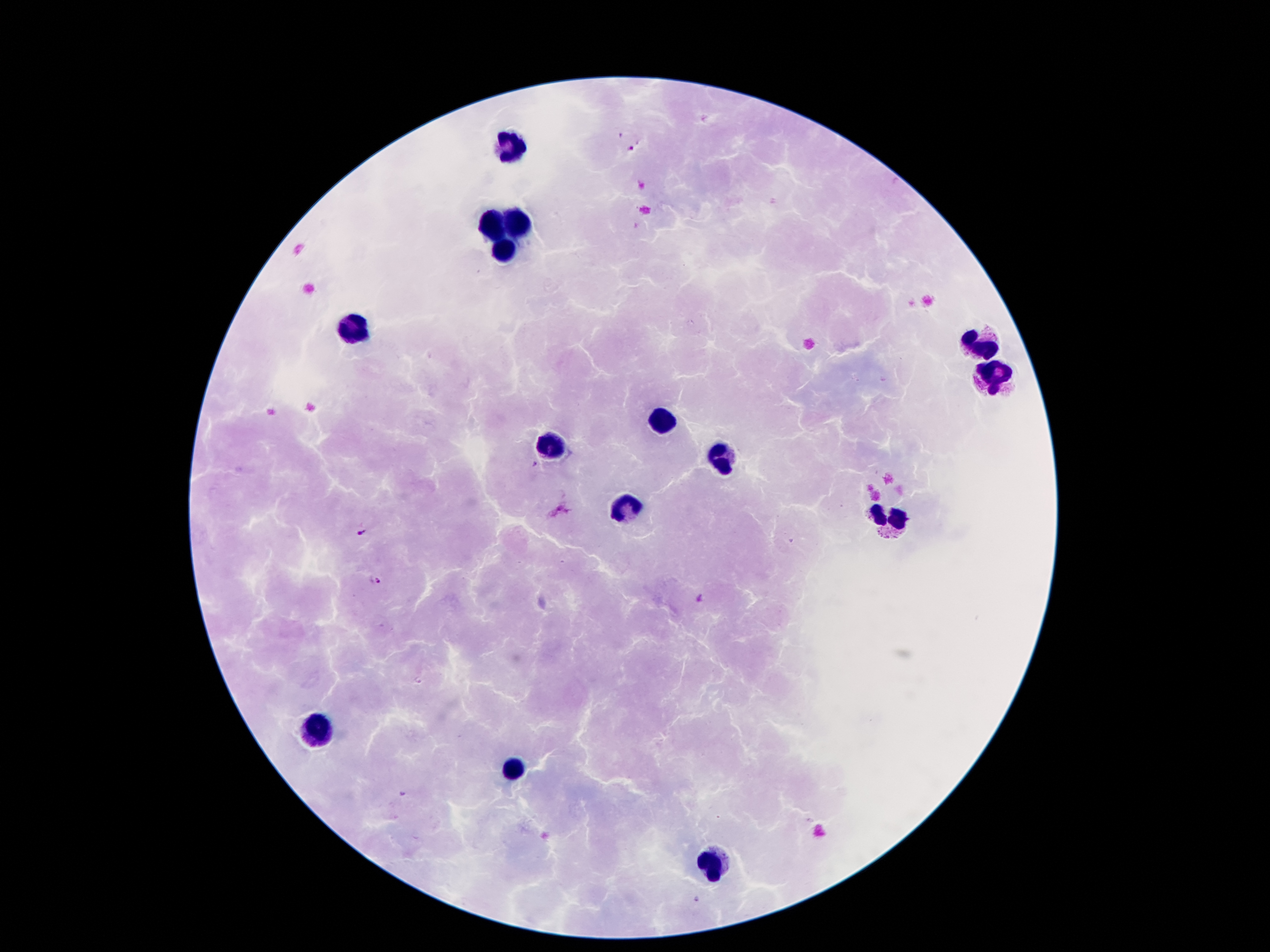 Approximate centers as [x, y] in pixels. Plasmodium parasite locations: [631, 149], [360, 533], [379, 582]. Leukocyte locations: [510, 144], [517, 220], [491, 226], [506, 248], [355, 326], [987, 349], [987, 375], [659, 420], [552, 448], [722, 457], [627, 509], [890, 519], [318, 725], [513, 767], [713, 863]. Giemsa-stained preparation. Smartphone photograph taken through the microscope eyepiece. Patient malaria status: infected with Plasmodium falciparum. Thick peripheral-blood smear. Image is 1270×952 pixels. Single field of view. 100x magnification.